Classify this cell by malaria status.
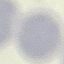
It is uninfected.

{
  "preparation": "thin blood film",
  "stain": "Giemsa",
  "image_type": "cell patch, automatically extracted from a larger field of view and resized to 64 × 64 pixels",
  "capture": "smartphone camera at the microscope eyepiece"
}